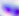

Photomicrograph. 400x magnification. Toxoplasma gondii is seen.